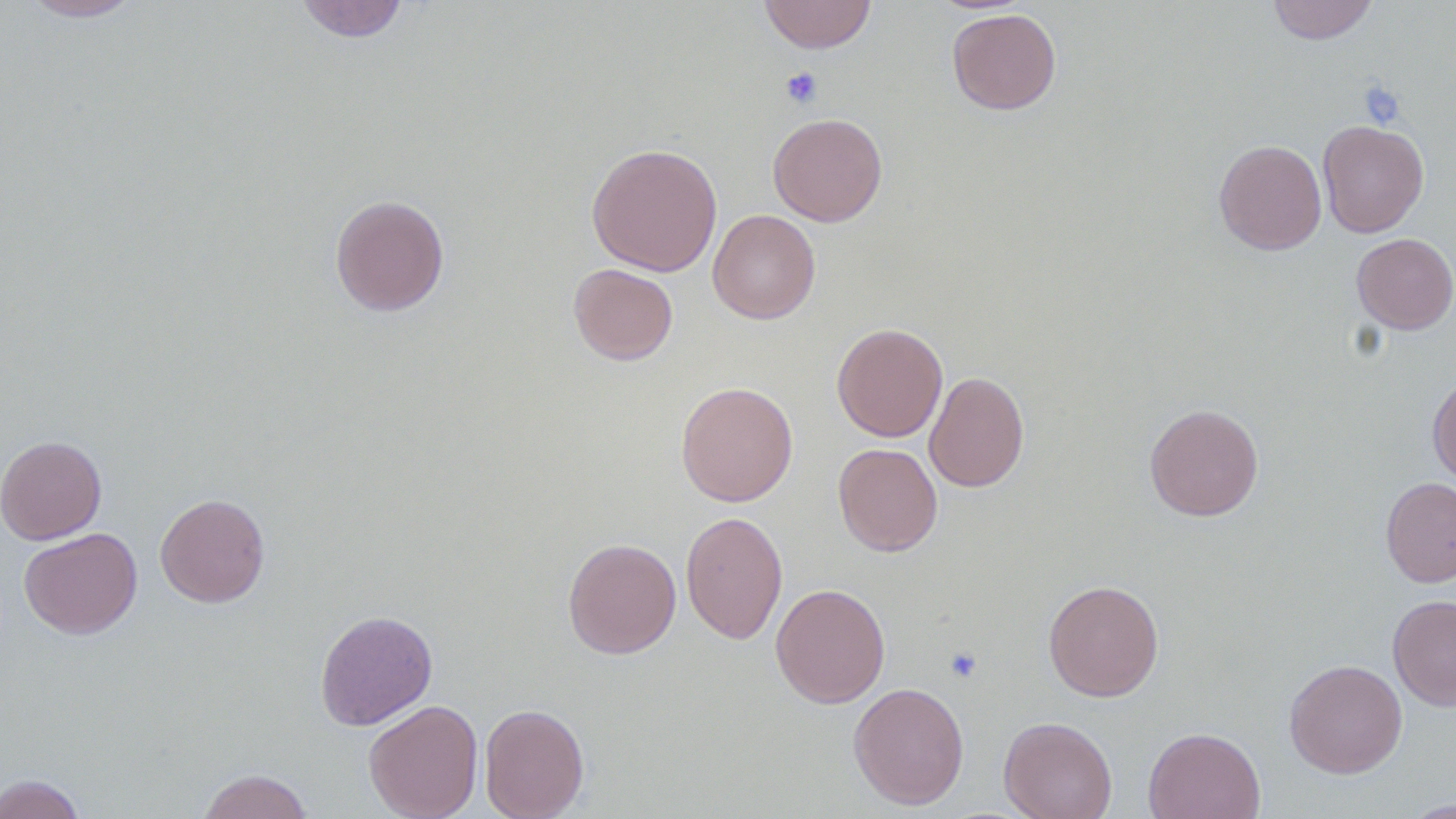 Approximate bounding boxes as (x1,y1)-(x2,y2) corner pairs in pixels. Uninfected red blood cell locations: (19,0)-(144,22), (295,0)-(411,43), (758,0)-(876,53), (1267,0)-(1377,45), (947,8)-(1062,115), (768,113)-(887,226), (1317,119)-(1429,237), (1214,139)-(1326,255), (586,142)-(723,276), (330,194)-(450,316), (707,209)-(821,324), (1352,233)-(1456,334), (568,263)-(678,365), (831,322)-(948,442), (924,371)-(1029,493), (1427,374)-(1456,486), (675,380)-(798,507), (1144,403)-(1264,521), (0,434)-(106,544), (833,442)-(943,557), (1379,477)-(1456,587), (155,492)-(270,608), (680,510)-(788,645), (19,527)-(143,639), (562,537)-(681,659), (1043,578)-(1164,702), (770,583)-(890,708), (1388,594)-(1456,711), (315,609)-(438,731), (1284,658)-(1407,778), (848,681)-(969,810), (363,699)-(483,819), (479,703)-(590,819), (999,715)-(1118,819), (1143,726)-(1266,819), (197,768)-(314,819), (0,773)-(87,819), (1401,798)-(1456,818). Platelet locations: (780,66)-(823,108), (1359,81)-(1406,129), (945,646)-(983,684). Slide-level diagnosis: negative for blood parasites. Light microscopy. 1000x magnification. Thin blood film. One field of a larger specimen. Image is 1456×819 pixels.